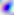
identification: Toxoplasma gondii
modality: micrograph
magnification: 400x